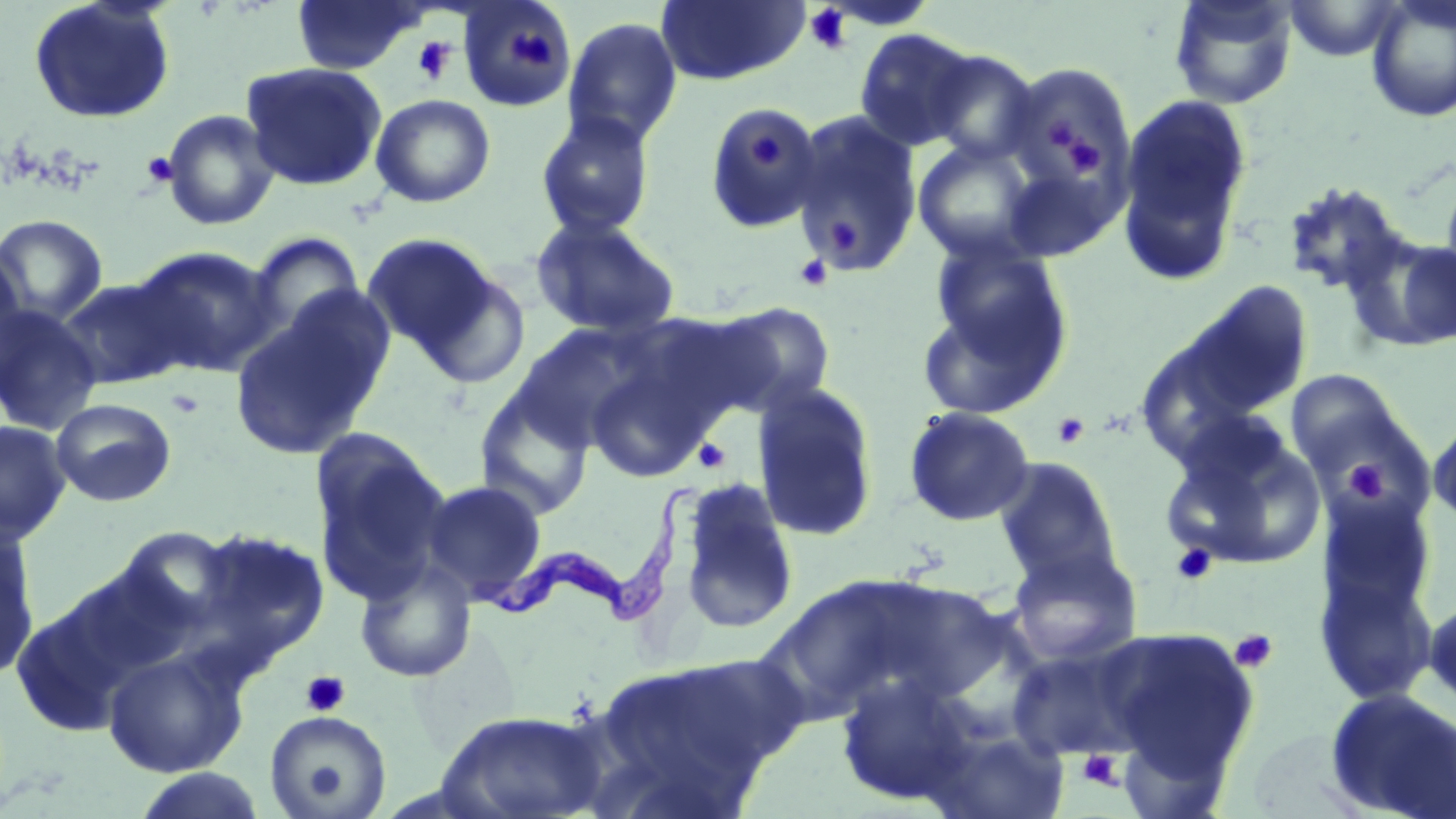
Summary:
  - Coordinate format: approximate bounding boxes as [x1, y1, x2, y2] in pixels
  - Uninfected red blood cell locations: [28, 0, 177, 125], [290, 0, 427, 75], [455, 0, 577, 113], [1168, 0, 1299, 109], [1364, 0, 1456, 123], [654, 1, 810, 86], [1282, 1, 1407, 62], [562, 17, 683, 150], [853, 28, 981, 151], [922, 50, 1041, 164], [240, 61, 388, 191], [999, 61, 1138, 213], [1115, 92, 1255, 284], [370, 93, 496, 208], [703, 104, 827, 235], [161, 109, 280, 231], [789, 111, 924, 277], [535, 112, 656, 238], [913, 140, 1044, 265], [1441, 163, 1456, 301], [1281, 180, 1411, 298], [0, 214, 108, 327], [530, 214, 682, 340], [243, 230, 366, 348], [1348, 231, 1456, 353], [361, 232, 500, 359], [924, 238, 1074, 388], [0, 241, 28, 383], [130, 245, 281, 376], [409, 268, 533, 390], [55, 277, 192, 390], [1169, 280, 1316, 424], [228, 294, 392, 461], [705, 301, 838, 417], [0, 304, 103, 435], [511, 326, 649, 451], [583, 353, 714, 484], [1283, 370, 1412, 489], [474, 379, 596, 520], [750, 382, 880, 542], [50, 398, 177, 507], [902, 406, 1036, 527], [1428, 416, 1456, 526], [0, 420, 71, 544], [1161, 420, 1327, 571], [308, 429, 451, 604], [993, 457, 1123, 588], [674, 477, 800, 633], [420, 479, 549, 606], [1315, 512, 1440, 709], [0, 521, 41, 682], [196, 527, 330, 659], [1005, 542, 1144, 668], [353, 558, 478, 683], [755, 574, 937, 725], [1424, 592, 1456, 714], [10, 595, 135, 738], [1099, 625, 1262, 790], [1005, 643, 1148, 761], [102, 647, 248, 778], [578, 653, 797, 818], [835, 672, 980, 808], [1322, 689, 1456, 819], [433, 708, 611, 819], [264, 710, 392, 818], [914, 720, 1072, 819], [131, 768, 268, 818]
  - Trypanosoma brucei locations: [469, 481, 699, 635]
  - Platelet locations: [803, 4, 855, 55], [507, 24, 555, 74], [411, 36, 457, 86], [1044, 115, 1092, 162], [749, 135, 783, 167], [1066, 136, 1102, 177], [140, 152, 177, 188], [823, 218, 864, 258], [794, 253, 833, 292], [165, 388, 205, 418], [1052, 412, 1091, 448], [693, 438, 731, 474], [1344, 458, 1389, 503], [1170, 543, 1219, 586], [1229, 629, 1278, 674], [301, 671, 350, 717], [1077, 750, 1124, 790]
  - Slide-level diagnosis: Trypanosoma brucei
  - Field of view: one of a larger specimen
  - Preparation: thin blood smear
  - Modality: light microscopy
  - Stain: May-Grünwald-Giemsa
  - Image size: 1456×819 pixels
  - Magnification: 1000x